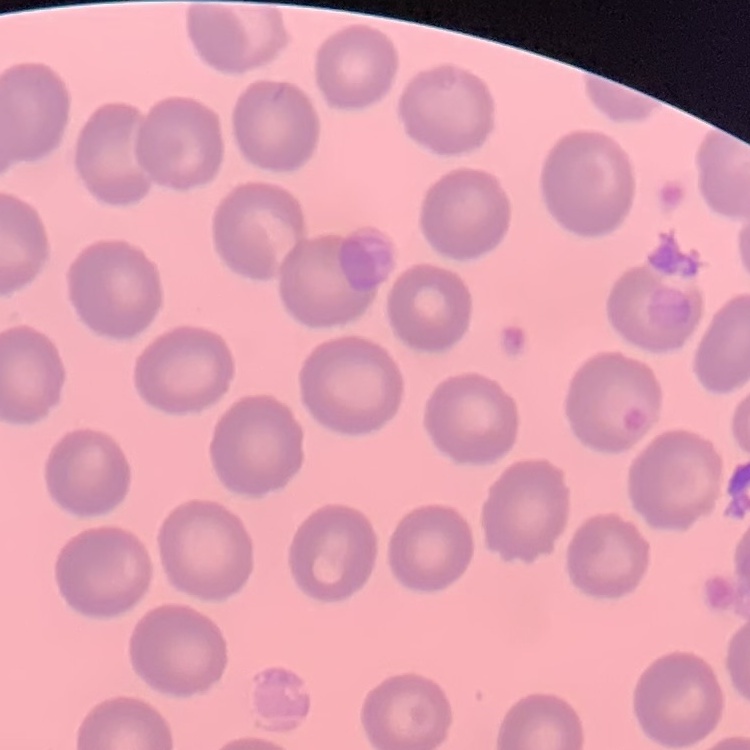
red_blood_cell_morphology: no rouleaux formation
preparation: thin peripheral smear
stain: Field's or Giemsa
image_type: square crop of a larger photomicrograph